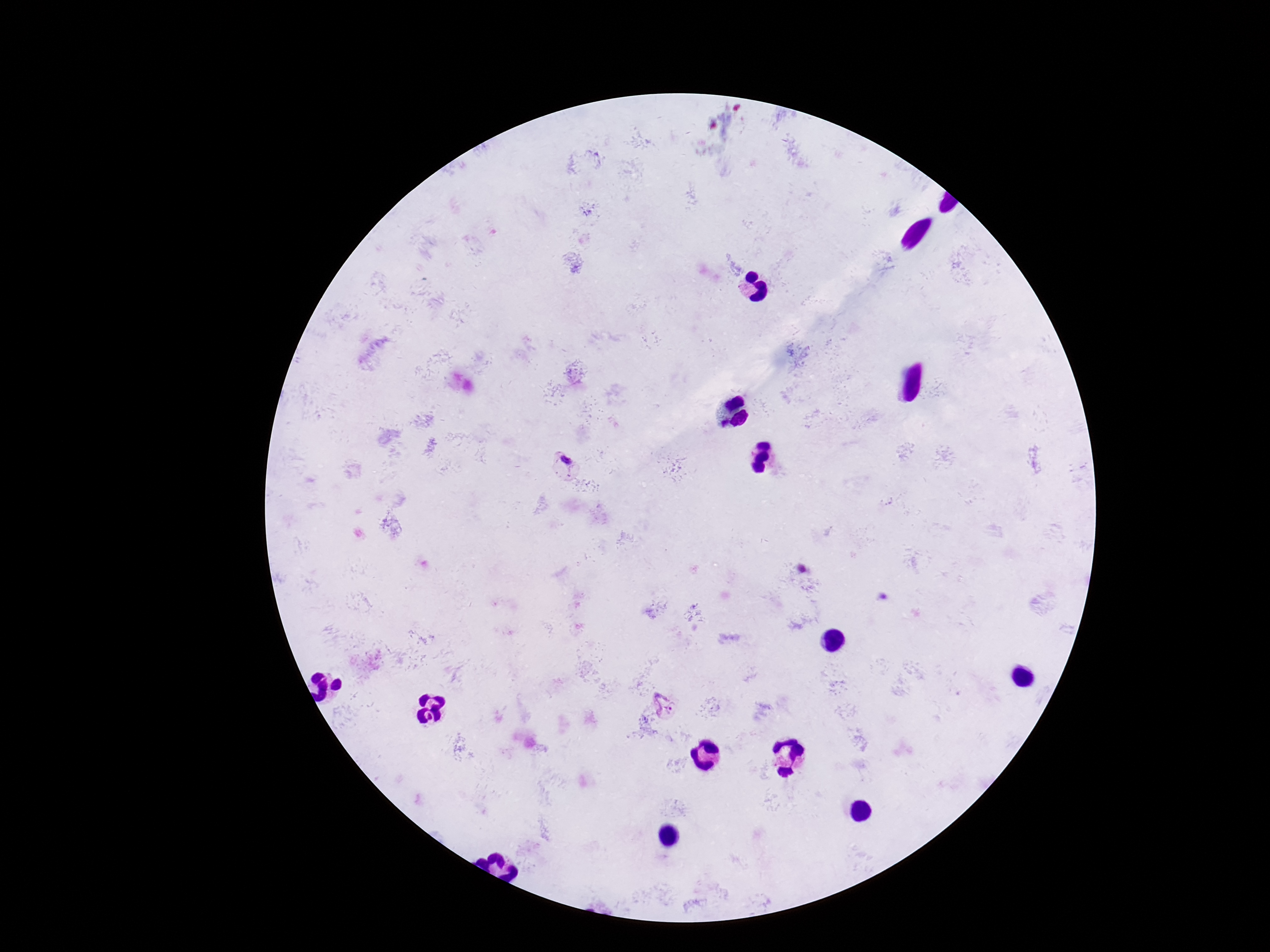 Approximate centers as {x, y} in pixels. Plasmodium parasite locations: {565, 462}, {665, 707}. Thick blood smear. Giemsa stain. Image is 1270×952 pixels. One field from this slide. Smartphone photograph taken through the microscope eyepiece. Patient malaria status: infected. 100x magnification.